Report the malaria status of this cell.
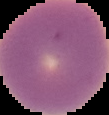
Uninfected.

Cell region segmented out of the field of view; the surrounding area is masked to black. Image is 109×115 pixels. From a thin blood film.